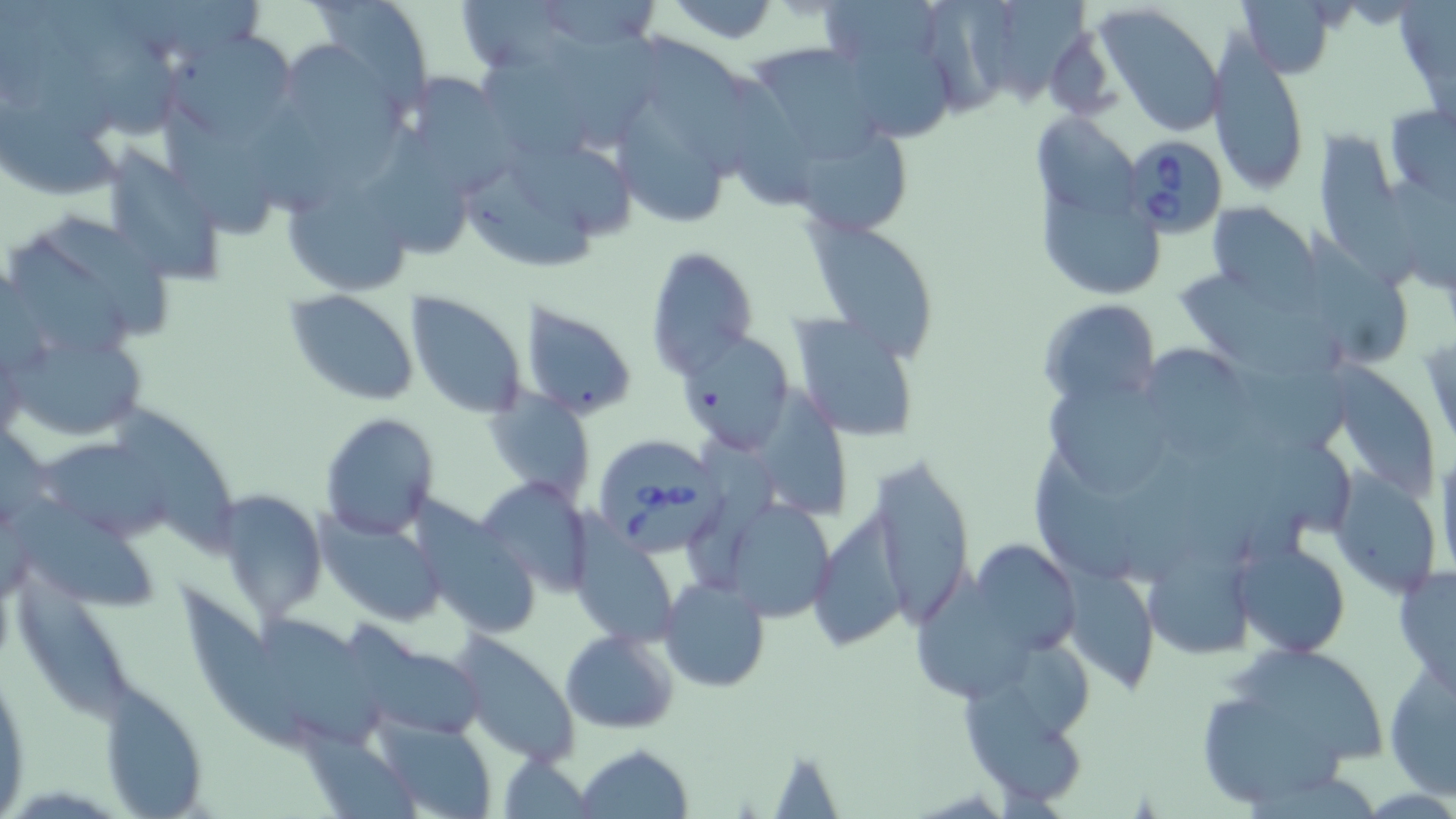 Approximate bounding boxes as [x1, y1, x2, y2] in pixels. Babesia divergens-infected red blood cell locations: [1128, 141, 1227, 238], [600, 442, 728, 553]. Uninfected red blood cell locations: [47, 0, 185, 140], [160, 0, 270, 57], [297, 0, 434, 115], [455, 0, 581, 74], [540, 0, 658, 47], [823, 0, 944, 62], [927, 0, 1017, 120], [1000, 0, 1086, 110], [1237, 0, 1338, 77], [660, 1, 786, 45], [1093, 3, 1226, 138], [550, 25, 655, 152], [163, 31, 301, 147], [643, 32, 757, 183], [844, 33, 958, 147], [1206, 34, 1310, 197], [483, 42, 602, 159], [286, 43, 408, 186], [747, 44, 884, 160], [409, 68, 517, 199], [716, 74, 824, 210], [155, 94, 276, 237], [619, 94, 729, 231], [0, 95, 125, 197], [1385, 105, 1455, 199], [361, 117, 467, 261], [1036, 117, 1143, 217], [1318, 125, 1420, 290], [803, 128, 913, 235], [505, 137, 633, 241], [98, 145, 227, 281], [1384, 166, 1456, 295], [470, 167, 605, 272], [285, 178, 413, 296], [1039, 188, 1161, 295], [1205, 199, 1317, 299], [19, 216, 171, 336], [807, 219, 936, 362], [1307, 226, 1412, 367], [645, 247, 756, 376], [1176, 266, 1329, 378], [286, 289, 419, 406], [405, 294, 526, 420], [1038, 300, 1161, 411], [518, 304, 637, 420], [788, 312, 920, 441], [678, 328, 794, 449], [10, 330, 147, 442], [1147, 341, 1249, 465], [1218, 348, 1359, 455], [1329, 367, 1442, 498], [752, 381, 849, 522], [1048, 386, 1169, 491], [486, 392, 597, 505], [115, 398, 241, 552], [320, 413, 439, 540], [688, 434, 789, 582], [1125, 435, 1227, 586], [1279, 435, 1355, 536], [41, 439, 183, 542], [1031, 444, 1151, 581], [1431, 448, 1456, 583], [869, 452, 976, 623], [1330, 473, 1443, 598], [479, 477, 594, 598], [4, 490, 161, 615], [219, 492, 327, 618], [737, 500, 836, 626], [808, 502, 919, 650], [318, 511, 446, 628], [423, 515, 543, 640], [573, 534, 677, 646], [965, 539, 1081, 658], [1144, 539, 1256, 660], [1233, 541, 1349, 657], [912, 557, 1046, 699], [1392, 562, 1456, 698], [1065, 567, 1161, 693], [11, 569, 141, 727], [659, 577, 770, 692], [181, 583, 309, 751], [264, 607, 382, 747], [560, 628, 680, 734], [453, 634, 581, 766], [958, 642, 1099, 813], [360, 643, 487, 737], [1227, 644, 1391, 766], [1383, 659, 1456, 801], [0, 665, 31, 811], [99, 684, 208, 818], [1210, 698, 1353, 804], [372, 715, 498, 819], [305, 733, 418, 819], [575, 744, 693, 819], [498, 755, 594, 817]. Slide-level diagnosis: Babesia divergens. Light microscopy. May-Grünwald-Giemsa stain. 1000x magnification. Image is 1456×819 pixels. Thin blood film. Single field of view.